Outline platelets.
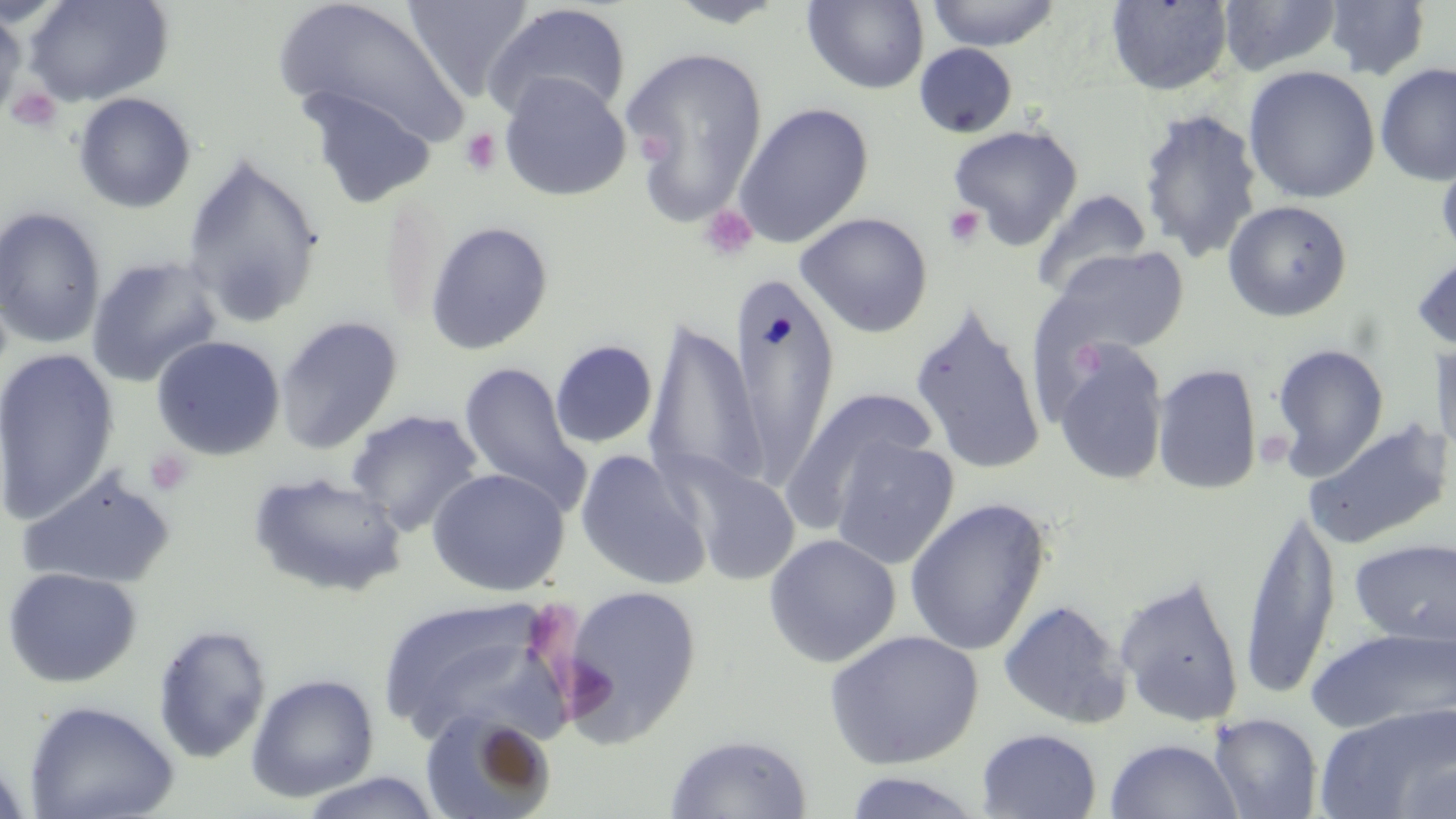

Approximate bounding boxes as [x1, y1, x2, y2] in pixels.
Platelets: [7, 86, 63, 133], [459, 128, 503, 176], [638, 133, 673, 164], [699, 204, 758, 262], [944, 206, 985, 248], [1071, 338, 1106, 378], [145, 449, 193, 497].

Summary:
  - Uninfected red blood cell locations: [23, 0, 175, 106], [272, 0, 471, 149], [403, 0, 534, 102], [663, 0, 792, 28], [1218, 0, 1343, 76], [802, 1, 929, 94], [926, 1, 1060, 51], [1105, 1, 1234, 95], [1324, 1, 1431, 81], [483, 3, 632, 125], [0, 7, 26, 124], [914, 43, 1018, 137], [622, 46, 769, 222], [1374, 62, 1456, 187], [1243, 65, 1381, 203], [498, 72, 632, 202], [299, 88, 437, 208], [73, 92, 196, 214], [733, 102, 874, 249], [1138, 108, 1263, 262], [948, 123, 1083, 249], [1436, 148, 1456, 269], [181, 153, 325, 328], [1032, 189, 1153, 299], [1222, 199, 1353, 322], [0, 206, 106, 349], [795, 211, 933, 337], [425, 221, 554, 355], [1046, 246, 1189, 358], [1410, 251, 1456, 352], [85, 255, 223, 387], [731, 270, 840, 487], [909, 302, 1046, 477], [275, 315, 404, 455], [645, 320, 765, 493], [150, 335, 286, 461], [1429, 336, 1456, 467], [550, 340, 658, 449], [1271, 342, 1389, 479], [1054, 343, 1168, 487], [0, 348, 119, 524], [458, 361, 585, 505], [1152, 363, 1262, 495], [781, 387, 937, 531], [345, 409, 484, 536], [1302, 418, 1453, 552], [828, 435, 960, 571], [574, 449, 712, 591], [678, 459, 801, 586], [17, 466, 177, 590], [427, 467, 571, 597], [247, 470, 407, 599], [904, 498, 1051, 657], [1239, 507, 1341, 697], [763, 533, 901, 668], [1349, 538, 1456, 647], [1, 567, 142, 688], [1114, 574, 1245, 727], [558, 584, 701, 745], [377, 595, 570, 745], [998, 599, 1132, 730], [152, 623, 273, 764], [1306, 627, 1455, 735], [823, 630, 984, 769], [245, 673, 380, 803], [23, 699, 180, 819], [1314, 704, 1456, 818], [417, 708, 556, 819], [1208, 713, 1323, 818], [977, 728, 1102, 819], [664, 733, 813, 818], [1104, 738, 1243, 819], [0, 756, 34, 819], [1392, 757, 1456, 818], [296, 771, 444, 818], [840, 771, 987, 818]
  - Slide-level diagnosis: no evidence of blood parasites
  - Field of view: single
  - Modality: optical microscopy
  - Magnification: 1000x
  - Stain: May-Grünwald-Giemsa
  - Preparation: thin blood film
  - Image size: 1456×819 pixels